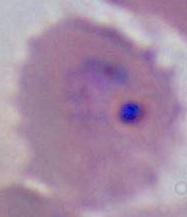

magnification = 400x or 1000x
modality = photomicrograph
identification = Plasmodium